Assess this cell for malaria.
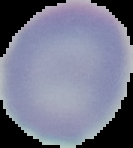

Uninfected.

Image is 133×148 pixels. Cell region segmented out of the field of view; the surrounding area is masked to black. From a thin blood film.